Identify the parasite.
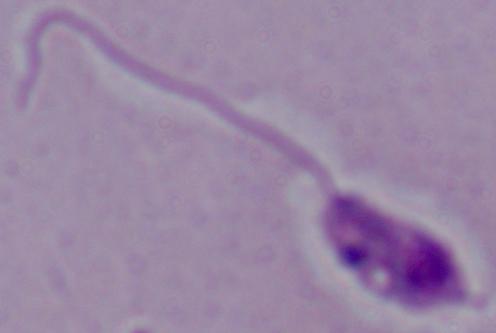

Leishmania.

magnification = 1000x
modality = micrograph